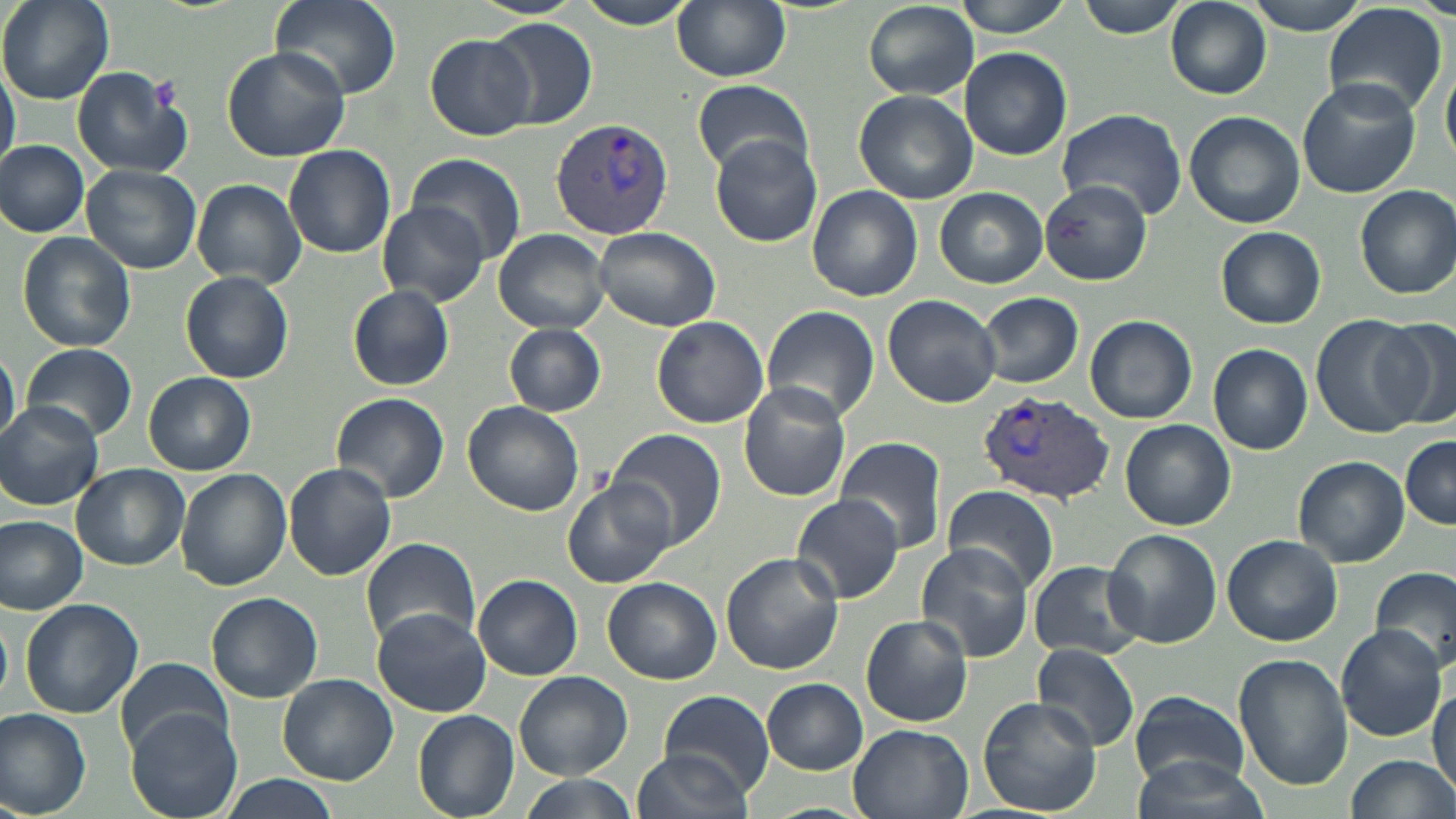

Summary:
  - Coordinate format: approximate bounding boxes as named x1/y1/x2/y2 corners in pixels
  - Platelet locations: (x1=150, y1=76, x2=183, y2=112)
  - Plasmodium vivax-infected red blood cell locations: (x1=550, y1=118, x2=674, y2=242), (x1=980, y1=391, x2=1116, y2=505)
  - Uninfected red blood cell locations: (x1=1, y1=0, x2=117, y2=104), (x1=270, y1=0, x2=401, y2=102), (x1=570, y1=0, x2=701, y2=29), (x1=672, y1=0, x2=790, y2=82), (x1=954, y1=0, x2=1073, y2=37), (x1=1076, y1=0, x2=1192, y2=39), (x1=1242, y1=0, x2=1372, y2=34), (x1=862, y1=2, x2=978, y2=101), (x1=1166, y1=2, x2=1272, y2=101), (x1=1321, y1=3, x2=1451, y2=119), (x1=487, y1=19, x2=598, y2=129), (x1=424, y1=33, x2=536, y2=140), (x1=221, y1=46, x2=350, y2=162), (x1=959, y1=47, x2=1071, y2=161), (x1=1442, y1=53, x2=1456, y2=168), (x1=0, y1=59, x2=18, y2=175), (x1=71, y1=67, x2=194, y2=180), (x1=1297, y1=77, x2=1422, y2=201), (x1=692, y1=79, x2=815, y2=175), (x1=854, y1=89, x2=978, y2=204), (x1=1056, y1=108, x2=1188, y2=220), (x1=1183, y1=111, x2=1305, y2=228), (x1=711, y1=133, x2=825, y2=249), (x1=0, y1=140, x2=90, y2=237), (x1=283, y1=144, x2=396, y2=257), (x1=409, y1=154, x2=525, y2=268), (x1=81, y1=164, x2=202, y2=274), (x1=192, y1=179, x2=306, y2=289), (x1=1042, y1=184, x2=1155, y2=288), (x1=1355, y1=184, x2=1456, y2=299), (x1=807, y1=185, x2=922, y2=301), (x1=935, y1=187, x2=1048, y2=288), (x1=377, y1=204, x2=487, y2=305), (x1=593, y1=226, x2=721, y2=331), (x1=1216, y1=226, x2=1327, y2=328), (x1=493, y1=229, x2=611, y2=333), (x1=16, y1=232, x2=137, y2=353), (x1=179, y1=270, x2=295, y2=384), (x1=347, y1=284, x2=457, y2=392), (x1=976, y1=292, x2=1084, y2=388), (x1=883, y1=293, x2=1001, y2=407), (x1=761, y1=305, x2=881, y2=424), (x1=1084, y1=314, x2=1198, y2=424), (x1=1311, y1=315, x2=1429, y2=437), (x1=651, y1=316, x2=770, y2=429), (x1=1369, y1=318, x2=1456, y2=428), (x1=503, y1=322, x2=607, y2=415), (x1=0, y1=343, x2=19, y2=452), (x1=1208, y1=343, x2=1314, y2=455), (x1=22, y1=344, x2=137, y2=441), (x1=143, y1=371, x2=254, y2=475), (x1=737, y1=381, x2=850, y2=501), (x1=331, y1=392, x2=449, y2=503), (x1=0, y1=401, x2=105, y2=509), (x1=460, y1=401, x2=584, y2=515), (x1=1120, y1=420, x2=1236, y2=530), (x1=608, y1=429, x2=727, y2=548), (x1=1399, y1=434, x2=1456, y2=529), (x1=836, y1=436, x2=947, y2=553), (x1=1293, y1=455, x2=1409, y2=568), (x1=282, y1=463, x2=396, y2=580), (x1=71, y1=464, x2=189, y2=571), (x1=175, y1=467, x2=291, y2=590), (x1=563, y1=477, x2=675, y2=588), (x1=940, y1=486, x2=1060, y2=593), (x1=793, y1=493, x2=905, y2=604), (x1=758, y1=512, x2=873, y2=636), (x1=0, y1=515, x2=88, y2=614), (x1=1101, y1=527, x2=1221, y2=648), (x1=1221, y1=535, x2=1342, y2=646), (x1=360, y1=536, x2=481, y2=650), (x1=915, y1=543, x2=1033, y2=662), (x1=720, y1=553, x2=844, y2=676), (x1=1027, y1=559, x2=1146, y2=661), (x1=1371, y1=566, x2=1455, y2=674), (x1=474, y1=575, x2=583, y2=681), (x1=602, y1=576, x2=722, y2=685), (x1=207, y1=592, x2=323, y2=703), (x1=20, y1=599, x2=143, y2=718), (x1=372, y1=608, x2=490, y2=717), (x1=861, y1=615, x2=973, y2=728), (x1=1335, y1=626, x2=1448, y2=741), (x1=1031, y1=642, x2=1138, y2=753), (x1=1234, y1=654, x2=1352, y2=792), (x1=115, y1=659, x2=235, y2=753), (x1=515, y1=671, x2=632, y2=780), (x1=278, y1=674, x2=398, y2=786), (x1=761, y1=678, x2=868, y2=774), (x1=1431, y1=680, x2=1455, y2=803), (x1=660, y1=689, x2=772, y2=795), (x1=1130, y1=691, x2=1249, y2=788), (x1=977, y1=697, x2=1103, y2=817), (x1=0, y1=707, x2=93, y2=818), (x1=127, y1=709, x2=243, y2=819), (x1=413, y1=710, x2=519, y2=818), (x1=847, y1=725, x2=974, y2=819), (x1=632, y1=745, x2=752, y2=819), (x1=1127, y1=750, x2=1273, y2=819), (x1=1342, y1=754, x2=1456, y2=819), (x1=221, y1=774, x2=334, y2=818), (x1=515, y1=775, x2=638, y2=819)
  - Slide-level diagnosis: Plasmodium vivax
  - Modality: optical microscopy
  - Magnification: 1000x
  - Image size: 1456×819 pixels
  - Preparation: thin blood smear
  - Field of view: single
  - Stain: May-Grünwald-Giemsa